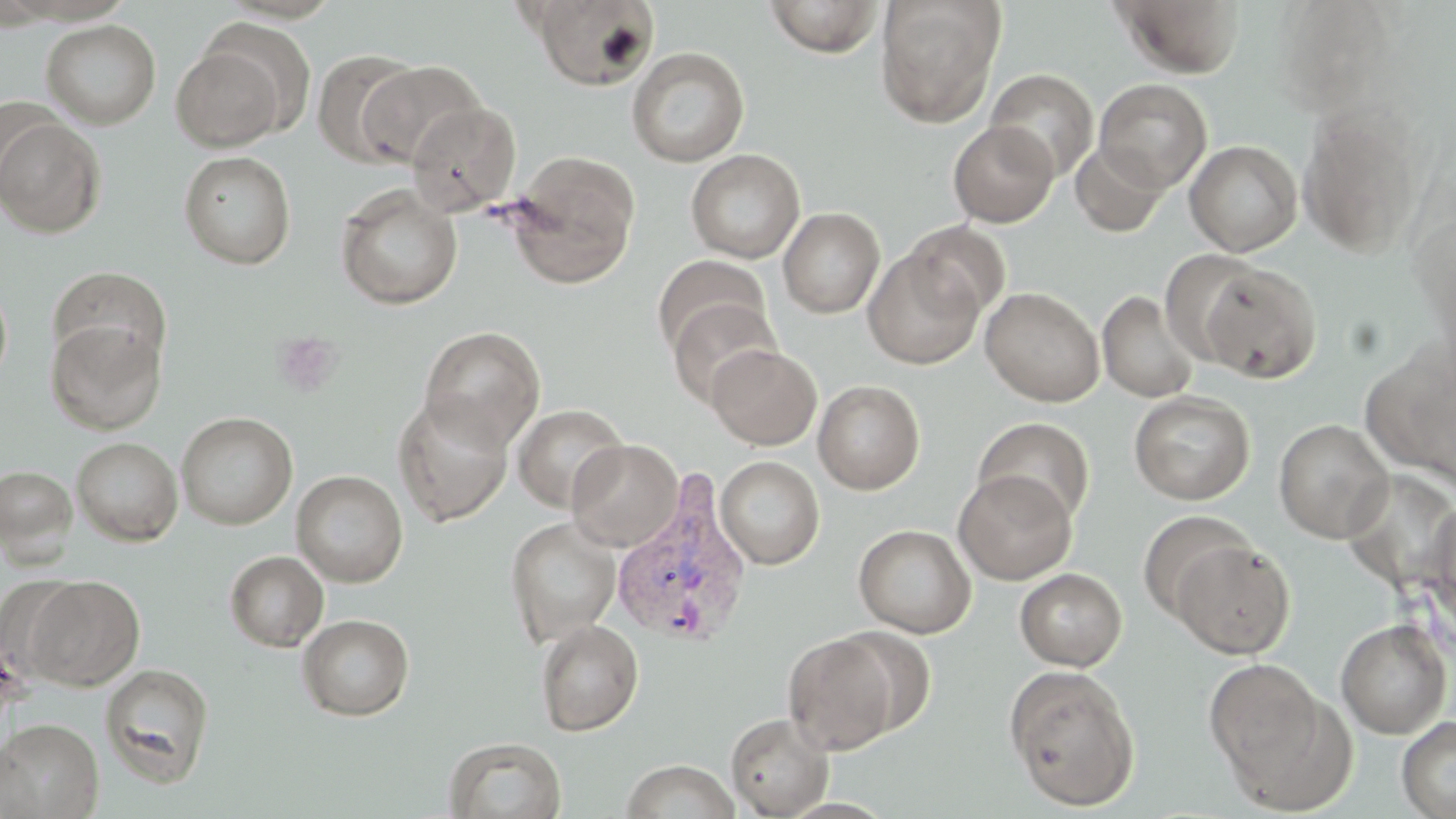
Approximate bounding boxes as (x1,y1)-(x2,y2) corner pairs in pixels. Plasmodium vivax-infected red blood cell locations: (609,474)-(755,648). Uninfected red blood cell locations: (528,0)-(660,91), (762,0)-(887,58), (875,0)-(1006,127), (1110,0)-(1246,79), (41,19)-(161,129), (170,42)-(289,150), (627,46)-(749,166), (312,49)-(423,167), (359,60)-(486,168), (985,68)-(1099,181), (1094,79)-(1212,192), (406,102)-(521,216), (1297,105)-(1425,259), (1,116)-(106,238), (948,121)-(1059,227), (1185,140)-(1302,257), (1070,141)-(1169,237), (686,148)-(805,264), (179,151)-(296,269), (504,151)-(641,289), (335,185)-(462,310), (778,207)-(885,318), (903,221)-(1011,323), (864,246)-(985,370), (1158,249)-(1263,365), (652,255)-(769,357), (1198,262)-(1323,383), (48,266)-(171,373), (0,277)-(13,392), (980,286)-(1105,406), (1097,290)-(1201,403), (666,298)-(780,408), (45,319)-(166,435), (419,326)-(546,451), (707,344)-(821,450), (813,379)-(925,494), (1129,390)-(1255,505), (393,393)-(514,526), (513,403)-(629,513), (176,411)-(298,530), (973,417)-(1095,525), (1273,418)-(1394,543), (72,437)-(183,546), (566,438)-(684,552), (715,456)-(825,569), (0,465)-(77,563), (291,470)-(408,587), (954,470)-(1076,584), (1428,497)-(1456,635), (1137,509)-(1255,622), (504,516)-(622,647), (853,524)-(976,637), (1170,538)-(1296,659), (225,550)-(328,652), (1015,568)-(1127,671), (24,575)-(144,690), (298,614)-(414,720), (536,619)-(644,736), (1335,619)-(1452,739), (832,627)-(938,736), (783,633)-(900,755), (1203,657)-(1333,799), (100,664)-(214,787), (1004,665)-(1141,811), (726,712)-(834,818), (1397,715)-(1456,819), (0,718)-(103,818), (443,736)-(566,819), (621,759)-(739,818). Platelet locations: (271,330)-(345,398). Slide-level diagnosis: Plasmodium vivax. Image is 1456×819 pixels. Single field of view. May-Grünwald-Giemsa-stained preparation. Optical microscopy. Captured at 1000x magnification. Thin blood film.